Report the malaria status of this cell.
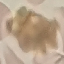

Uninfected.

{
  "stain": "Giemsa",
  "image_type": "cell patch, automatically extracted from a larger field of view and resized to 64 × 64 pixels",
  "preparation": "thin smear",
  "capture": "smartphone through the microscope eyepiece"
}